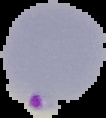
The area outside the segmented cell region is set to black. From a thin blood film. Image is 106×118 pixels. Result: Plasmodium parasites detected.